Give the position of every leukocyte visible.
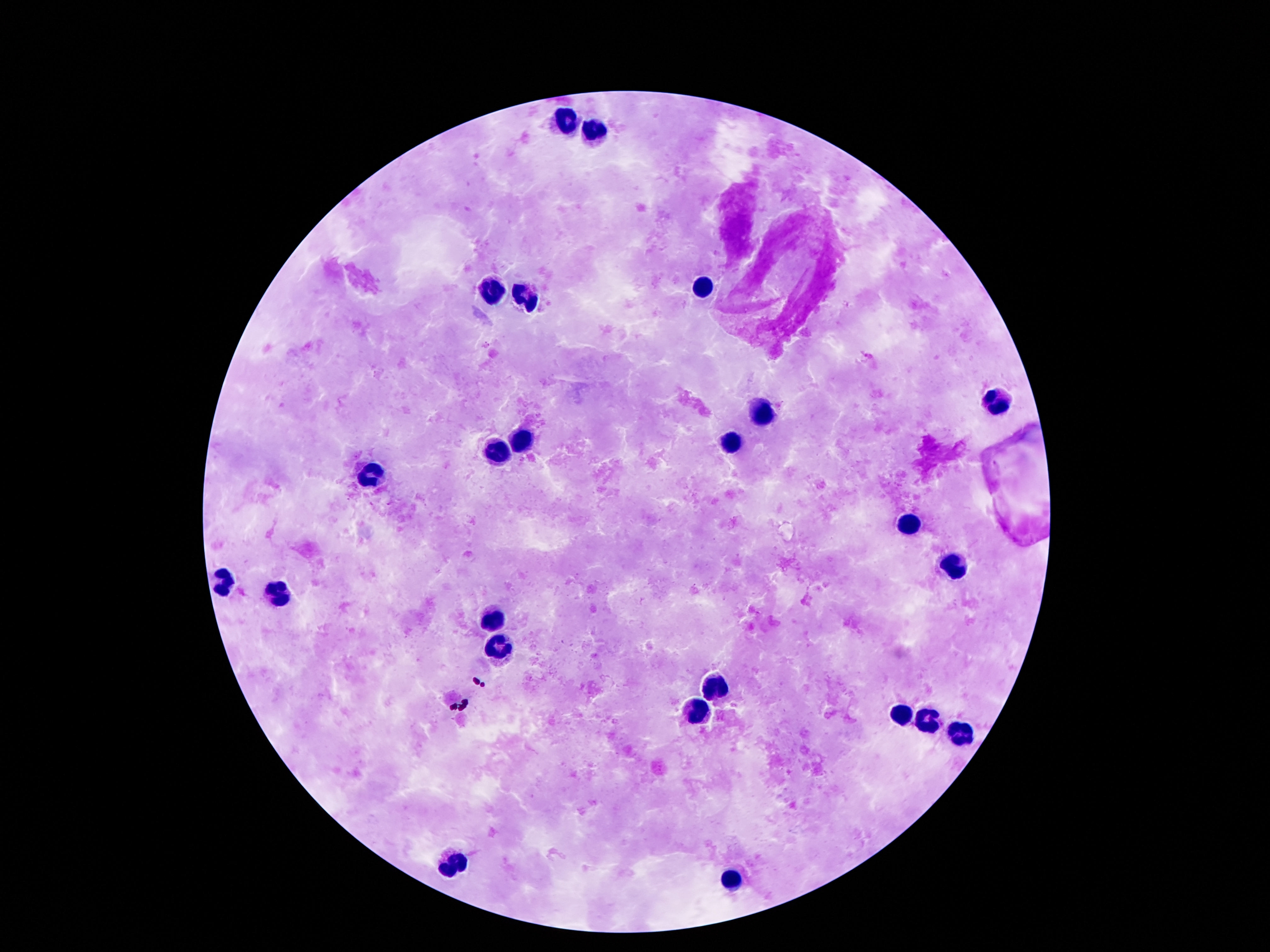
Approximate centers as [x, y] in pixels.
Leukocytes: [563, 122], [590, 133], [699, 288], [492, 294], [528, 300], [992, 404], [760, 410], [730, 444], [519, 445], [501, 454], [370, 478], [912, 522], [955, 562], [222, 585], [279, 599], [492, 619], [501, 649], [715, 688], [696, 710], [899, 713], [928, 721], [958, 733], [454, 863], [730, 880].

capture = smartphone camera through the microscope eyepiece
preparation = thick blood smear
stain = Giemsa
image size = 1270×952 pixels
field of view = one from this slide
magnification = 100x
patient malaria status = not infected